Report the malaria status of this cell.
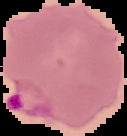

It is parasitized.

Summary:
  - Image size: 127×136 pixels
  - Image type: segmented cell region with the area outside set to black
  - Preparation: thin blood smear